Comment on the morphology of the erythrocytes.
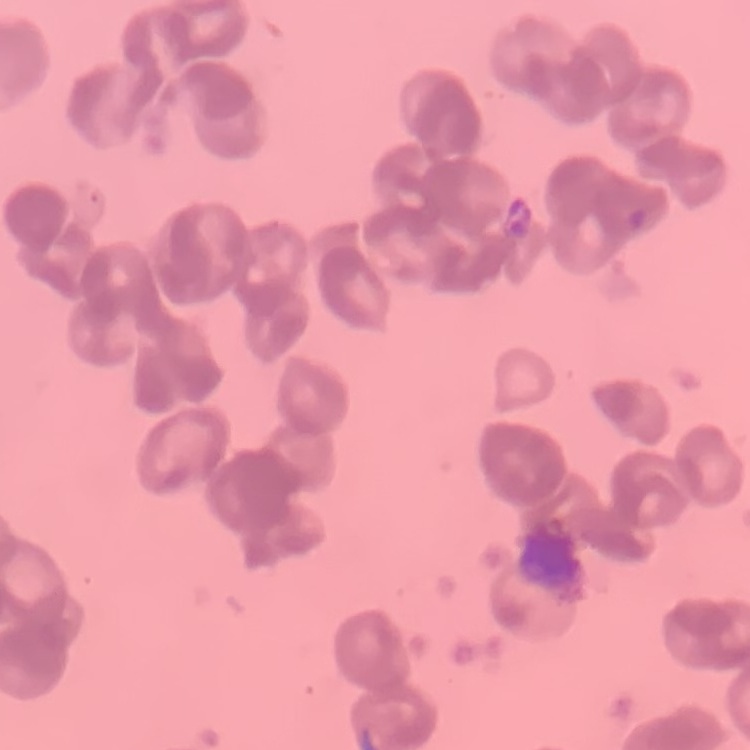

Rouleaux formation.

Summary:
  - Preparation: thin blood smear
  - Stain: Field's or Giemsa
  - Image type: one tile cut from a larger photomicrograph